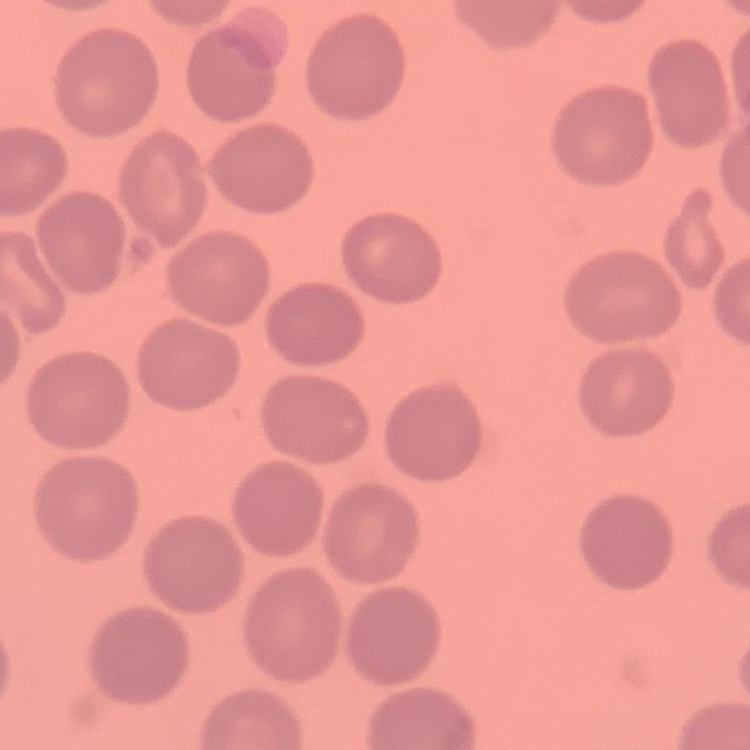

Summary:
  - Red blood cell morphology: no rouleaux formation
  - Preparation: thin blood film
  - Stain: Field's or Giemsa
  - Image type: square crop of a larger photomicrograph